Name the parasite shown.
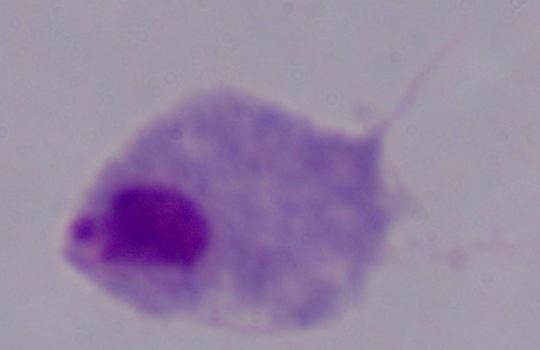

A trichomonad.

Micrograph. 1000x magnification.